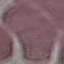
Summary:
  - Malaria status: uninfected
  - Capture: smartphone through the microscope eyepiece
  - Preparation: thin blood smear
  - Image type: cell patch, automatically extracted from a larger field of view and resized to 64 × 64 pixels
  - Stain: Giemsa